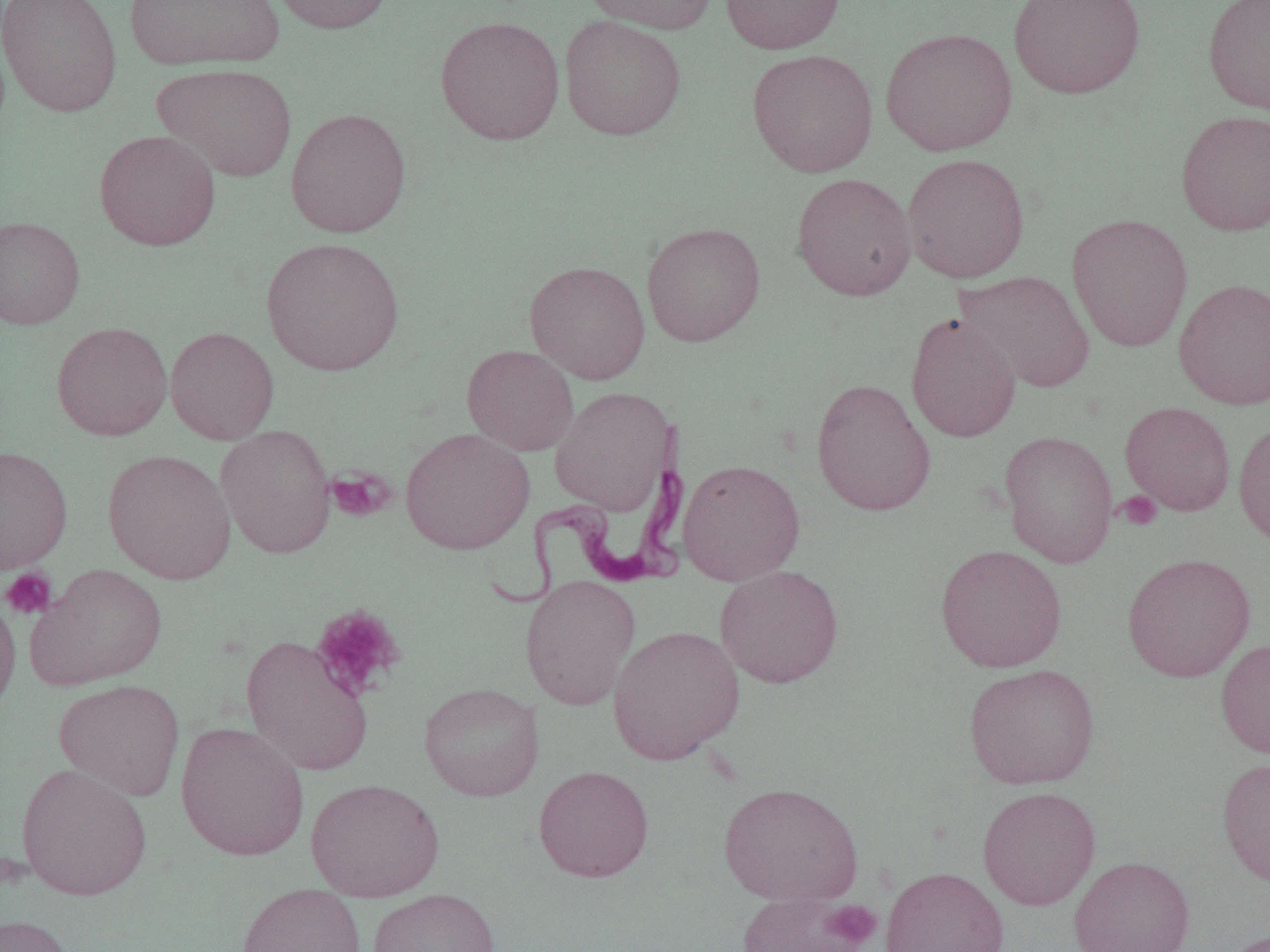

slide_level_diagnosis: Trypanosoma brucei
field_of_view: single
preparation: thin blood smear
uninfected_red_blood_cell_locations: 'approximate bounding boxes as named x1/y1/x2/y2 corners in pixels: (x1=1, y1=0, x2=122, y2=116), (x1=267, y1=0, x2=395, y2=35), (x1=582, y1=0, x2=719, y2=35), (x1=721, y1=0, x2=844, y2=54), (x1=1008, y1=0, x2=1146, y2=99), (x1=1203, y1=0, x2=1270, y2=116), (x1=124, y1=1, x2=285, y2=71), (x1=435, y1=15, x2=565, y2=145), (x1=559, y1=15, x2=686, y2=140), (x1=880, y1=27, x2=1017, y2=156), (x1=747, y1=48, x2=879, y2=177), (x1=154, y1=63, x2=298, y2=182), (x1=285, y1=107, x2=411, y2=238), (x1=1175, y1=110, x2=1270, y2=236), (x1=94, y1=129, x2=221, y2=250), (x1=902, y1=152, x2=1030, y2=283), (x1=791, y1=172, x2=917, y2=301), (x1=1067, y1=213, x2=1193, y2=352), (x1=0, y1=216, x2=85, y2=329), (x1=641, y1=222, x2=766, y2=347), (x1=261, y1=236, x2=404, y2=377), (x1=525, y1=260, x2=650, y2=384), (x1=954, y1=270, x2=1096, y2=394), (x1=1173, y1=277, x2=1270, y2=410), (x1=905, y1=311, x2=1022, y2=443), (x1=51, y1=321, x2=173, y2=441), (x1=165, y1=326, x2=279, y2=445), (x1=462, y1=344, x2=579, y2=455), (x1=811, y1=378, x2=937, y2=517), (x1=550, y1=386, x2=675, y2=516), (x1=1119, y1=401, x2=1236, y2=516), (x1=1233, y1=420, x2=1270, y2=548), (x1=215, y1=424, x2=336, y2=559), (x1=400, y1=427, x2=535, y2=555), (x1=999, y1=429, x2=1119, y2=567), (x1=0, y1=444, x2=73, y2=574), (x1=103, y1=449, x2=236, y2=584), (x1=677, y1=459, x2=805, y2=586), (x1=935, y1=543, x2=1068, y2=673), (x1=1122, y1=552, x2=1256, y2=683), (x1=25, y1=563, x2=168, y2=691), (x1=715, y1=565, x2=845, y2=688), (x1=520, y1=574, x2=641, y2=710), (x1=0, y1=592, x2=21, y2=718), (x1=608, y1=624, x2=745, y2=765), (x1=240, y1=634, x2=374, y2=776), (x1=1215, y1=638, x2=1270, y2=760), (x1=964, y1=663, x2=1100, y2=789), (x1=53, y1=679, x2=185, y2=801), (x1=419, y1=682, x2=544, y2=801), (x1=175, y1=721, x2=309, y2=861), (x1=1217, y1=757, x2=1270, y2=889), (x1=16, y1=762, x2=152, y2=901), (x1=533, y1=765, x2=654, y2=882), (x1=306, y1=777, x2=444, y2=902), (x1=718, y1=781, x2=864, y2=907), (x1=977, y1=786, x2=1100, y2=910), (x1=1068, y1=856, x2=1195, y2=951), (x1=881, y1=866, x2=1010, y2=952), (x1=236, y1=882, x2=366, y2=952), (x1=368, y1=888, x2=500, y2=952), (x1=737, y1=889, x2=875, y2=952), (x1=0, y1=914, x2=75, y2=952), (x1=1220, y1=928, x2=1270, y2=952)'
modality: optical microscopy
magnification: 1000x
platelet_locations: 'approximate bounding boxes as named x1/y1/x2/y2 corners in pixels: (x1=326, y1=467, x2=395, y2=522), (x1=1117, y1=491, x2=1162, y2=529), (x1=0, y1=567, x2=57, y2=620), (x1=310, y1=604, x2=406, y2=700), (x1=825, y1=899, x2=881, y2=950)'
trypanosoma_brucei_locations: 'approximate bounding boxes as named x1/y1/x2/y2 corners in pixels: (x1=485, y1=428, x2=690, y2=612)'
image_size: 1270×952 pixels